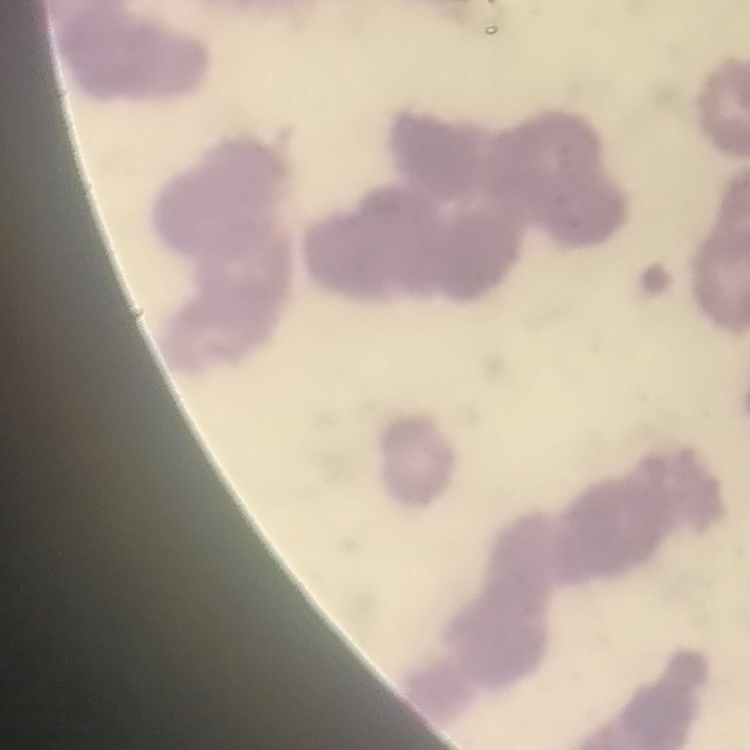 The red blood cells exhibit rouleaux formation. Thin blood film. Square crop of a larger photomicrograph. Stained with either Field's or Giemsa.